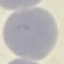
malaria status = uninfected
preparation = thin blood smear
stain = Giemsa
image type = automatically extracted cell patch, resized to 64 × 64 pixels
capture = smartphone camera at the microscope eyepiece